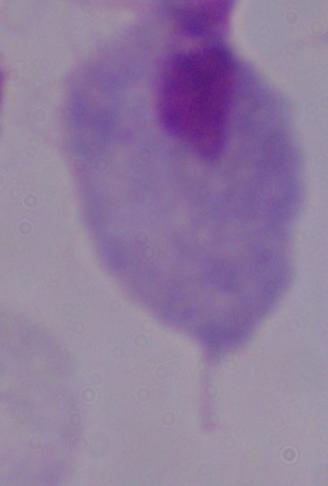
magnification = 1000x
modality = micrograph
identification = trichomonad